Describe the morphology of the erythrocytes.
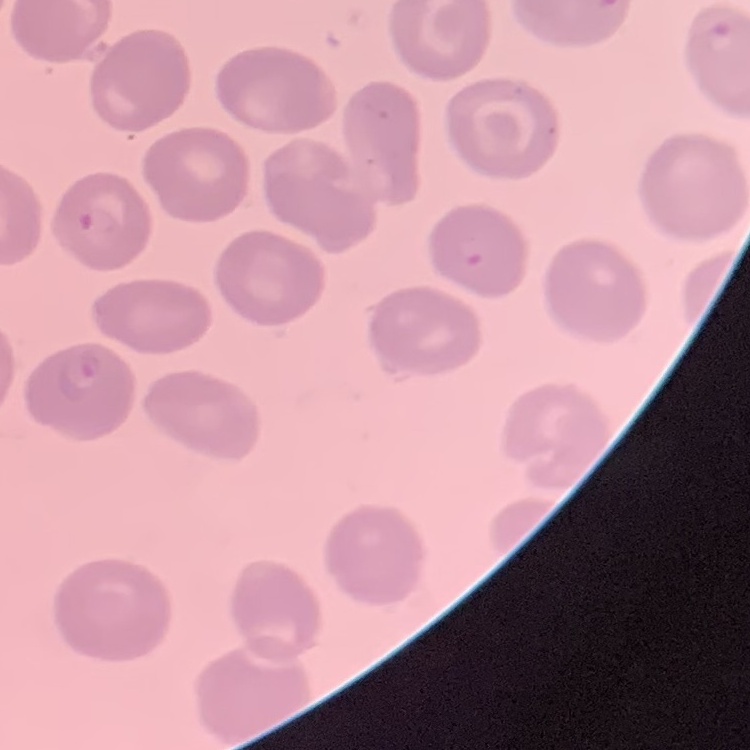
No rouleaux formation.

stain = Field's or Giemsa
image type = one tile cut from a larger photomicrograph
preparation = thin blood film